Identify the parasite.
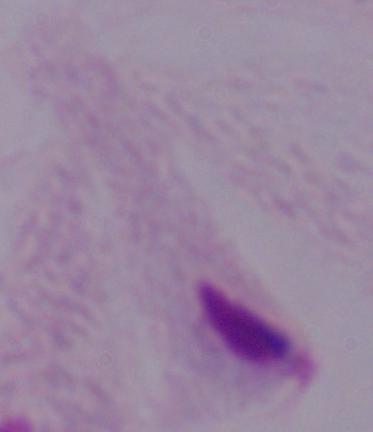
This is a trichomonad.

Summary:
  - Modality: micrograph
  - Magnification: 1000x